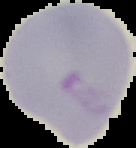

From a thin blood smear. The area outside the segmented cell region is set to black. Image is 136×148 pixels. Malaria status: parasitized.